Comment on the morphology of the erythrocytes.
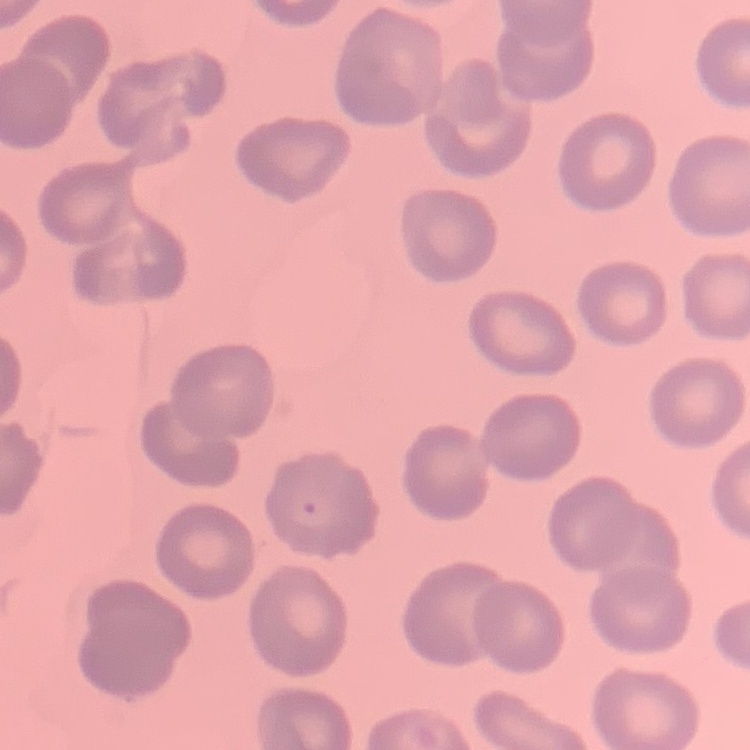
They show no rouleaux formation.

One tile cut from a larger photomicrograph. Thin blood smear. Field's or Giemsa stain.